State which parasite is depicted.
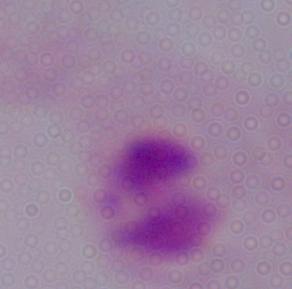

A trichomonad.

{
  "modality": "photomicrograph",
  "magnification": "1000x"
}